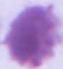 An erythrocyte is shown. Micrograph. Captured at 1000x magnification.